Outline each uninfected red blood cell.
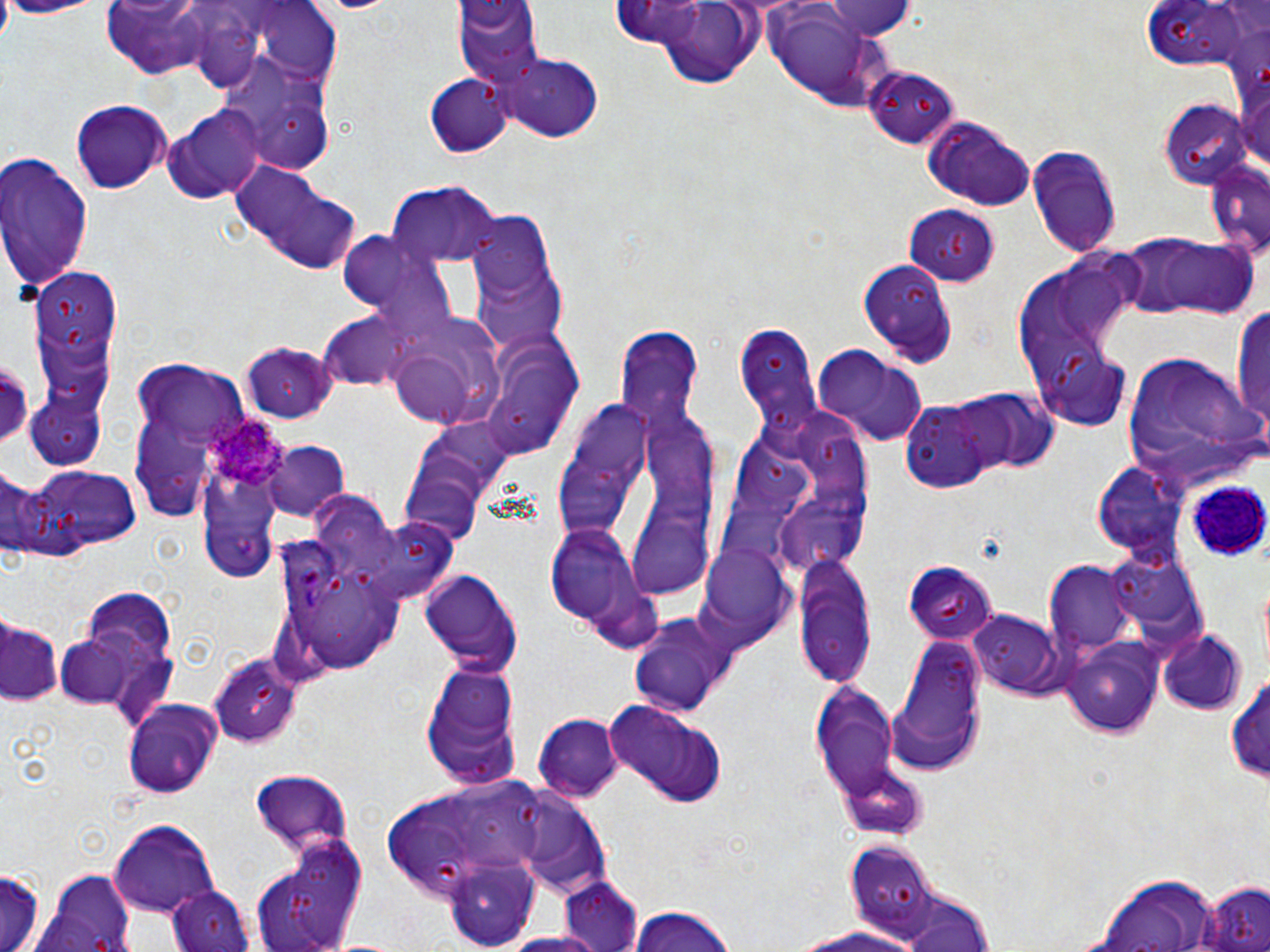
Approximate bounding boxes as (x1, y1, x2, y2) in pixels.
Uninfected red blood cells: (0, 0, 106, 19), (258, 0, 341, 69), (455, 0, 543, 90), (670, 0, 753, 91), (1142, 0, 1242, 73), (819, 2, 918, 40), (100, 3, 227, 79), (781, 14, 864, 105), (498, 53, 604, 142), (865, 67, 959, 149), (228, 69, 338, 173), (426, 71, 513, 159), (69, 99, 172, 193), (1159, 101, 1255, 189), (166, 106, 268, 200), (918, 115, 1035, 213), (1027, 143, 1121, 260), (0, 155, 92, 289), (231, 162, 362, 275), (1204, 162, 1269, 259), (385, 183, 504, 265), (903, 204, 1000, 285), (461, 207, 566, 354), (338, 231, 442, 320), (1115, 236, 1205, 318), (1160, 239, 1259, 317), (858, 259, 959, 368), (1012, 259, 1135, 414), (34, 266, 128, 353), (1232, 300, 1270, 441), (316, 311, 420, 394), (383, 315, 503, 427), (731, 319, 821, 437), (615, 325, 704, 426), (239, 341, 337, 424), (811, 346, 930, 447), (1119, 348, 1262, 488), (1039, 350, 1133, 432), (137, 360, 248, 445), (505, 365, 580, 445), (553, 386, 719, 603), (954, 388, 1058, 475), (897, 393, 1011, 493), (33, 400, 101, 464), (734, 408, 872, 577), (261, 436, 348, 522), (1090, 460, 1186, 557), (15, 465, 142, 556), (0, 470, 53, 556), (402, 480, 474, 554), (203, 512, 277, 582), (358, 515, 458, 607), (545, 521, 656, 648), (700, 545, 797, 644), (1107, 548, 1205, 637), (791, 554, 878, 687), (1045, 561, 1134, 656), (905, 563, 995, 643), (416, 566, 522, 677), (312, 573, 387, 675), (80, 589, 180, 671), (628, 607, 743, 720), (967, 608, 1076, 702), (1, 613, 64, 705), (1155, 630, 1247, 716), (52, 631, 161, 718), (1061, 634, 1165, 738), (887, 637, 986, 775), (208, 652, 303, 746), (420, 663, 523, 789), (1228, 671, 1270, 786), (807, 676, 906, 814), (604, 700, 728, 807), (121, 701, 224, 797), (534, 715, 622, 801), (834, 764, 928, 841), (250, 770, 352, 862), (380, 775, 553, 900), (516, 796, 610, 901), (110, 820, 218, 919), (253, 837, 371, 951), (845, 843, 940, 937), (445, 859, 539, 948), (2, 867, 44, 952), (29, 869, 142, 952), (1089, 874, 1222, 950), (557, 877, 645, 952), (1202, 881, 1269, 952), (169, 884, 254, 952), (898, 894, 994, 952), (623, 906, 741, 952), (785, 921, 926, 951), (497, 932, 610, 952).

Summary:
  - White blood cell locations: (1184, 478, 1269, 558)
  - Plasmodium ovale-infected red blood cell locations: (200, 408, 284, 489)
  - Slide-level diagnosis: Plasmodium ovale
  - Image size: 1270×952 pixels
  - Stain: May-Grünwald-Giemsa
  - Modality: optical microscopy
  - Magnification: 1000x
  - Field of view: single
  - Preparation: thin blood film